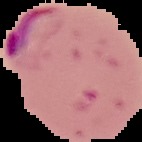
Summary:
  - Preparation: thin blood smear
  - Malaria status: parasitized
  - Image size: 142×142 pixels
  - Image type: segmented cell region on a black background